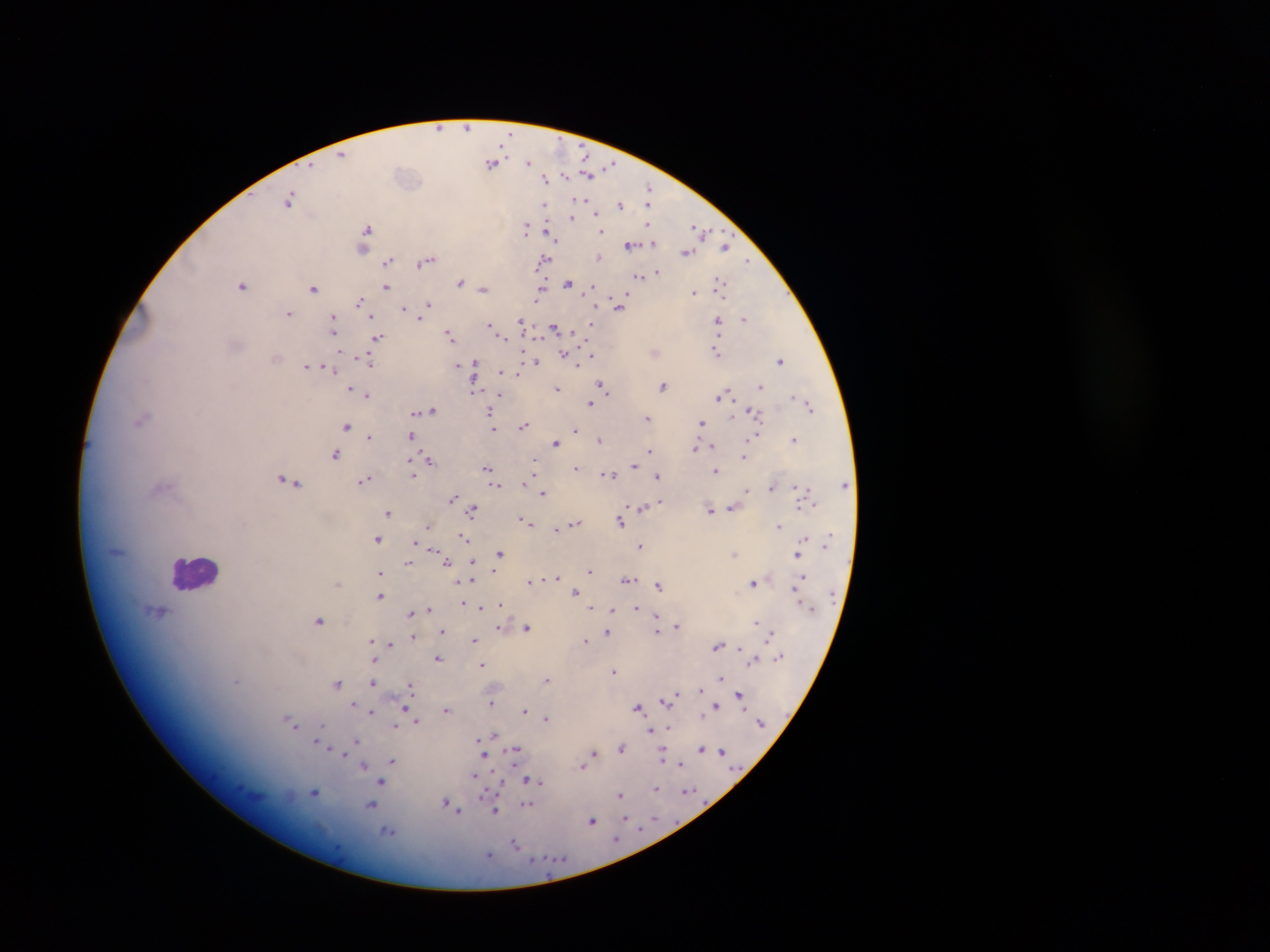

leukocyte_locations: 'approximate centers as x y in pixels: 195 572'
plasmodium_parasite_locations: 'approximate centers as x y in pixels: 439 127; 467 127; 342 154; 529 162; 493 163; 610 166; 588 173; 566 175; 546 178; 649 190; 289 199; 579 201; 620 204; 545 205; 650 205; 596 212; 573 217; 527 227; 366 230; 701 231; 601 232; 549 233; 364 241; 653 241; 631 245; 726 246; 363 248; 686 252; 600 258; 544 259; 427 260; 388 261; 747 261; 657 272; 640 275; 461 281; 721 282; 568 283; 243 285; 387 287; 314 288; 484 288; 591 288; 540 290; 693 292; 360 299; 428 304; 619 305; 404 309; 289 313; 370 315; 421 317; 594 318; 744 318; 718 320; 522 322; 592 323; 490 324; 334 325; 555 327; 451 334; 502 336; 378 337; 716 350; 565 354; 591 354; 276 357; 367 360; 781 360; 536 362; 475 363; 578 364; 457 365; 307 366; 331 370; 501 371; 475 372; 519 375; 760 384; 603 386; 664 386; 350 388; 474 388; 557 388; 368 394; 728 394; 721 396; 496 400; 591 403; 810 405; 433 410; 490 411; 753 411; 415 413; 648 418; 141 420; 703 422; 524 425; 347 426; 494 429; 576 429; 370 436; 411 436; 756 436; 600 439; 795 439; 556 442; 695 446; 711 446; 649 449; 335 454; 744 456; 429 460; 536 460; 634 465; 576 466; 412 467; 535 468; 487 469; 717 471; 415 474; 609 474; 657 475; 365 479; 525 479; 287 480; 846 484; 163 486; 496 486; 773 486; 799 487; 747 489; 543 493; 452 498; 661 500; 813 503; 800 505; 732 507; 642 508; 473 509; 710 509; 388 511; 523 519; 621 520; 577 522; 780 526; 557 529; 804 537; 378 538; 464 538; 416 542; 640 544; 432 549; 799 552; 499 553; 734 554; 447 561; 408 562; 473 562; 591 571; 380 572; 804 576; 558 577; 627 580; 472 581; 529 581; 456 582; 338 583; 754 583; 658 585; 575 590; 796 592; 380 595; 501 603; 480 606; 593 607; 429 608; 613 608; 636 608; 159 612; 410 613; 657 616; 320 620; 756 623; 677 626; 500 627; 527 627; 658 630; 443 631; 607 633; 771 633; 414 637; 371 638; 474 639; 585 640; 391 645; 718 645; 740 647; 438 658; 754 658; 374 661; 482 663; 614 671; 721 677; 546 679; 236 680; 338 683; 373 683; 410 685; 701 688; 679 692; 739 694; 674 696; 665 701; 491 702; 354 704; 715 704; 639 707; 741 708; 405 709; 447 709; 525 710; 372 712; 702 714; 546 717; 416 720; 293 724; 322 725; 395 725; 669 726; 651 731; 494 733; 481 740; 316 742; 357 742; 355 746; 622 747; 703 747; 514 750; 722 750; 483 754; 594 754; 663 754; 345 755; 586 759; 393 760; 365 764; 682 764; 582 766; 473 775; 530 779; 382 781; 539 783; 656 788; 688 790; 314 792; 621 795; 483 796; 448 803; 372 805; 527 805; 496 810; 624 818; 655 819; 592 820; 616 837; 516 844; 489 854'
preparation: thick blood film
field_of_view: single
capture: mobile-phone photograph through a microscope
image_size: 1270×952 pixels
country: Ghana